Name the parasite shown.
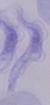
A trypanosome.

Summary:
  - Modality: photomicrograph
  - Magnification: 1000x